Identify the parasite.
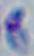

This is Toxoplasma gondii.

Captured at 1000x magnification. Photomicrograph.